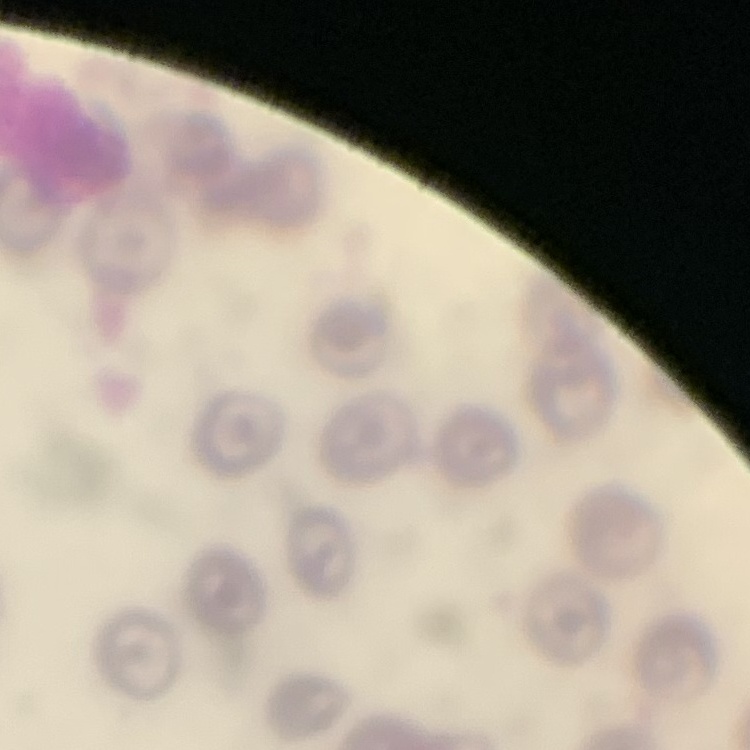

red blood cell morphology = no rouleaux formation
stain = Field's or Giemsa
preparation = thin peripheral smear
image type = one tile cut from a larger photomicrograph